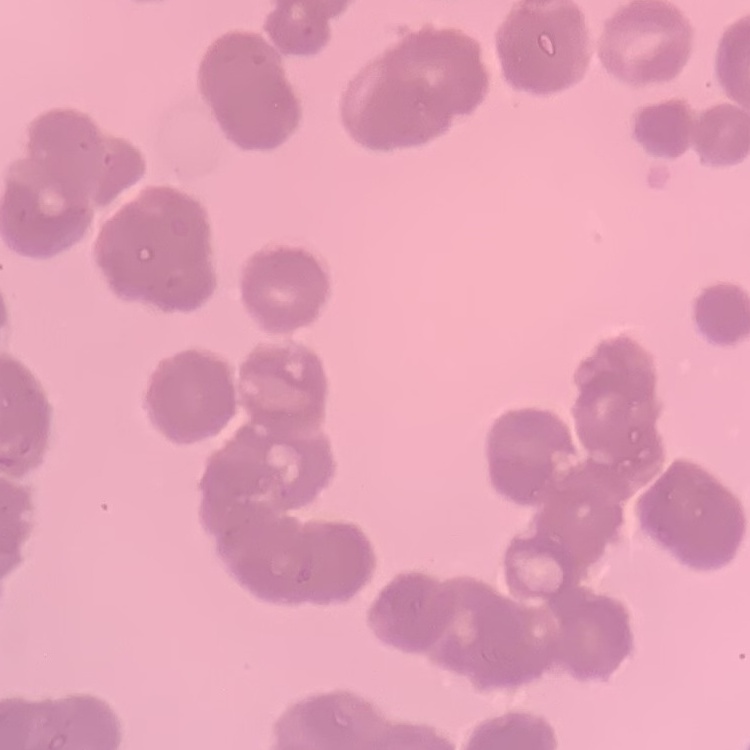
The erythrocytes exhibit rouleaux formation. Thin blood smear. Stained with either Field's or Giemsa. Square crop of a larger photomicrograph.